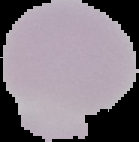

Summary:
  - Preparation: thin blood smear
  - Image size: 139×142 pixels
  - Image type: segmented cell region on a black background
  - Result: no Plasmodium parasites detected